Comment on the morphology of the erythrocytes.
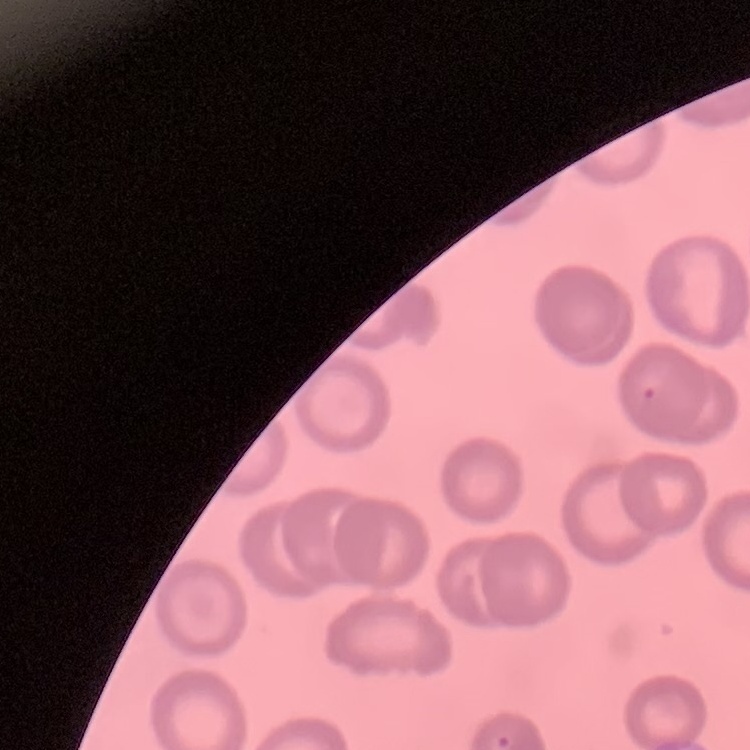

No rouleaux formation.

Field's or Giemsa stain. Thin peripheral smear. Square crop of a larger photomicrograph.